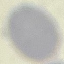

result = negative for malaria parasites
preparation = thin blood film
image type = automatically extracted cell patch, resized to 64 × 64 pixels
stain = Giemsa
capture = smartphone through the microscope eyepiece